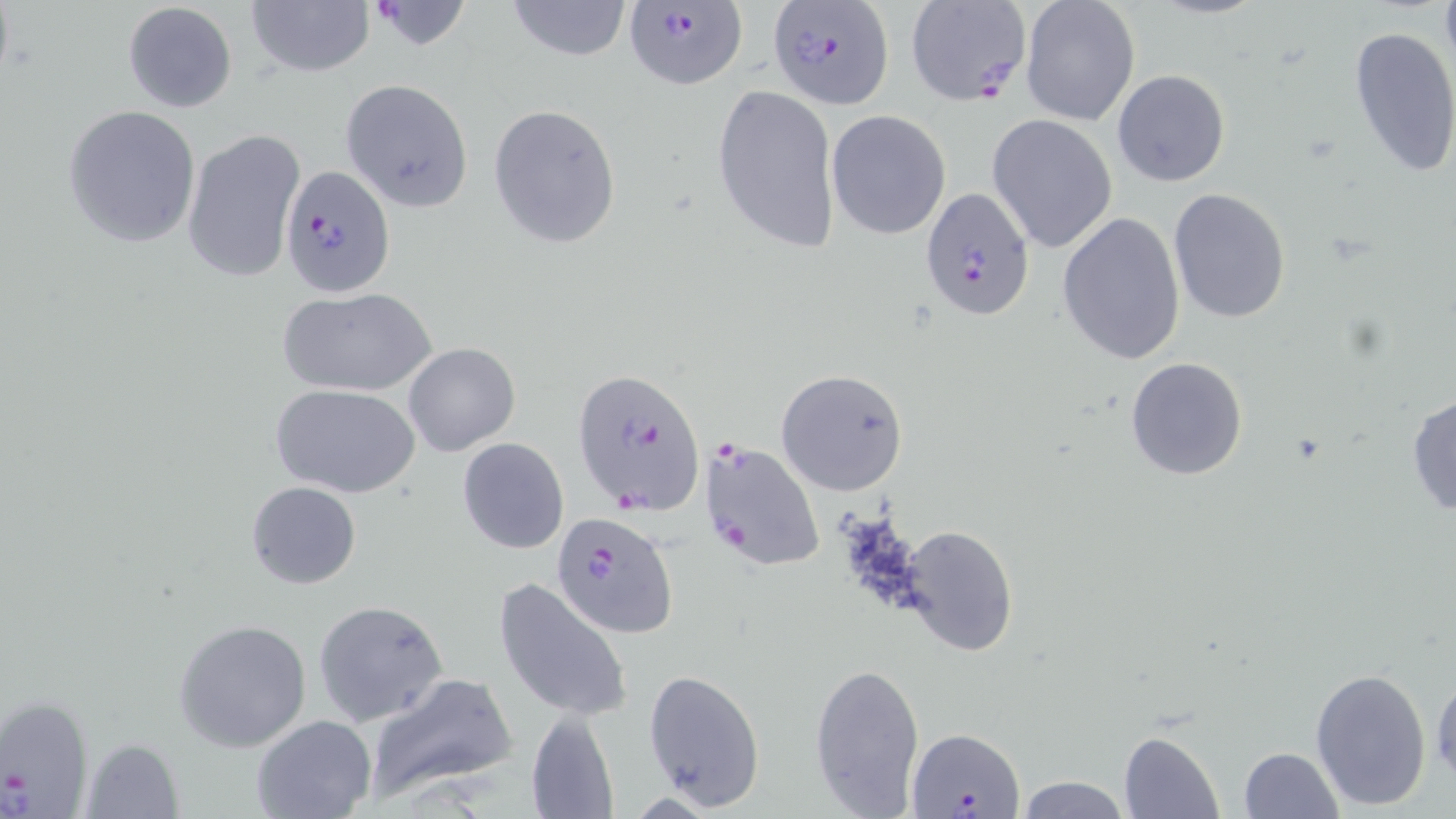
slide_level_diagnosis: Plasmodium falciparum
uninfected_red_blood_cell_locations: 'approximate bounding boxes as (x1, y1, x2, y2) in pixels: (508, 0, 632, 60), (1020, 0, 1141, 126), (121, 1, 238, 113), (247, 2, 375, 78), (1347, 26, 1456, 180), (1111, 68, 1231, 187), (342, 79, 474, 210), (711, 83, 841, 255), (486, 103, 622, 249), (62, 106, 202, 248), (826, 110, 951, 240), (987, 113, 1118, 253), (181, 128, 305, 284), (1168, 188, 1291, 324), (1057, 211, 1187, 366), (280, 285, 435, 397), (404, 342, 520, 456), (1125, 356, 1249, 481), (777, 368, 911, 496), (273, 385, 419, 498), (1407, 392, 1456, 518), (458, 438, 569, 555), (246, 481, 361, 589), (900, 526, 1019, 657), (493, 577, 632, 721), (314, 601, 448, 726), (174, 620, 313, 752), (809, 660, 926, 817), (1430, 666, 1455, 786), (1309, 668, 1432, 812), (642, 669, 765, 811), (362, 672, 518, 805), (525, 710, 619, 819), (251, 714, 377, 819), (1119, 731, 1225, 819), (79, 736, 184, 817), (1237, 747, 1343, 819), (1015, 775, 1130, 818)'
preparation: thin blood film
magnification: 1000x
stain: May-Grünwald-Giemsa
modality: optical microscopy
field_of_view: single
plasmodium_falciparum_infected_red_blood_cell_locations: 'approximate bounding boxes as (x1, y1, x2, y2) in pixels: (364, 0, 474, 52), (904, 0, 1033, 108), (620, 2, 749, 91), (767, 3, 895, 110), (281, 165, 396, 295), (920, 187, 1035, 319), (574, 367, 706, 513), (699, 439, 825, 573), (551, 511, 678, 639), (0, 693, 93, 817), (907, 726, 1023, 816)'
image_size: 1456×819 pixels